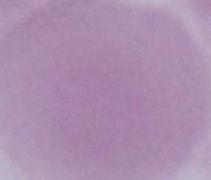
Summary:
  - Magnification: 1000x
  - Identification: erythrocyte
  - Modality: photomicrograph